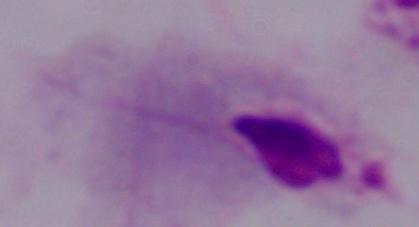
Summary:
  - Modality: photomicrograph
  - Identification: trichomonad
  - Magnification: 1000x